Locate every Plasmodium malariae-infected red blood cell.
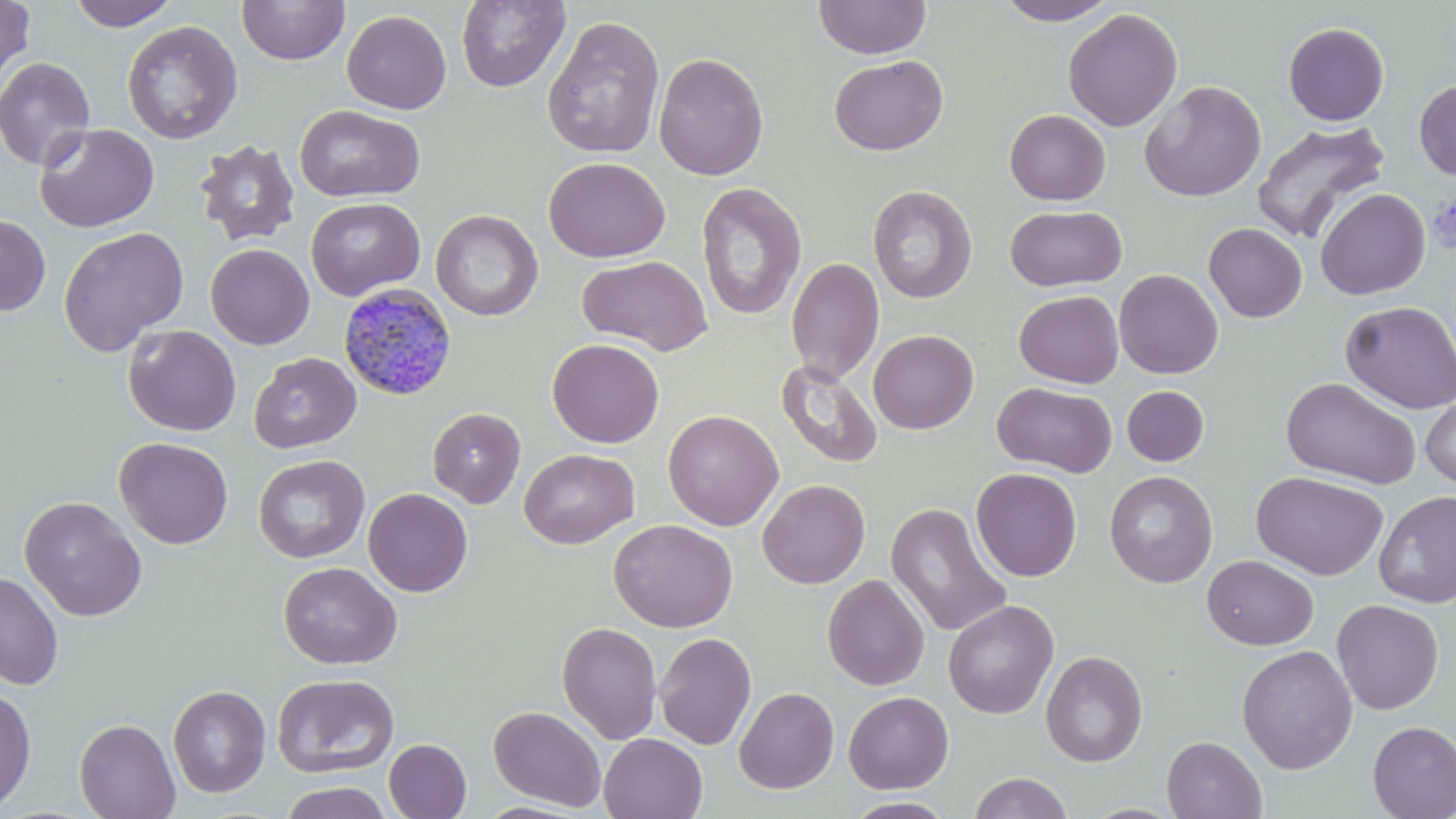
Approximate bounding boxes as (x1,y1)-(x2,y2) corner pairs in pixels.
Plasmodium malariae-infected red blood cells: (338,282)-(457,401).

slide-level diagnosis = Plasmodium malariae
field of view = one of a larger specimen
preparation = thin blood film
modality = optical microscopy
image size = 1456×819 pixels
platelet locations = approximate bounding boxes as (x1,y1)-(x2,y2) corner pairs in pixels: (1427,194)-(1456,253)
uninfected red blood cell locations = approximate bounding boxes as (x1,y1)-(x2,y2) corner pairs in pixels: (0,0)-(35,87), (67,0)-(181,30), (237,0)-(349,65), (814,0)-(931,59), (995,0)-(1118,25), (455,1)-(571,93), (1063,7)-(1183,132), (341,9)-(452,114), (543,15)-(666,158), (122,20)-(243,145), (1283,22)-(1389,126), (653,52)-(769,181), (829,54)-(948,155), (0,56)-(96,170), (1414,79)-(1456,181), (1139,80)-(1266,202), (295,104)-(425,203), (1004,109)-(1111,205), (1252,120)-(1390,244), (35,123)-(159,232), (193,139)-(301,247), (544,157)-(670,262), (696,182)-(806,320), (868,185)-(977,303), (1315,188)-(1430,300), (305,196)-(425,300), (1005,205)-(1127,292), (431,209)-(543,321), (0,213)-(50,316), (1203,223)-(1307,322), (57,225)-(189,357), (205,244)-(314,349), (577,254)-(713,355), (785,257)-(885,384), (1114,268)-(1224,379), (1014,290)-(1124,388), (1340,301)-(1456,414), (123,324)-(241,436), (868,329)-(979,434), (547,339)-(664,448), (248,352)-(361,454), (775,360)-(883,468), (1281,376)-(1420,489), (993,382)-(1117,478), (1122,386)-(1209,466), (1420,390)-(1456,489), (427,407)-(526,508), (663,409)-(784,530), (114,437)-(233,549), (519,448)-(639,548), (253,454)-(369,563), (970,468)-(1082,582), (1104,470)-(1218,588), (1251,471)-(1389,580), (757,479)-(871,588), (363,488)-(473,597), (1374,490)-(1456,608), (20,495)-(147,621), (885,503)-(1012,637), (609,519)-(737,632), (1202,555)-(1318,650), (278,561)-(402,669), (0,570)-(64,690), (822,574)-(930,690), (942,599)-(1059,719), (1332,599)-(1444,715), (556,621)-(662,744), (654,632)-(757,750), (1237,644)-(1358,775), (1041,650)-(1148,767), (271,672)-(400,778), (0,684)-(36,813), (168,685)-(270,797), (734,686)-(839,794), (843,691)-(954,794), (76,700)-(271,807), (488,705)-(606,811), (74,717)-(180,819), (1367,721)-(1456,819), (599,733)-(708,819), (1161,736)-(1267,818), (384,738)-(472,818), (969,772)-(1072,819), (278,780)-(395,819), (842,797)-(958,818), (473,800)-(594,818)
magnification = 1000x
stain = May-Grünwald-Giemsa